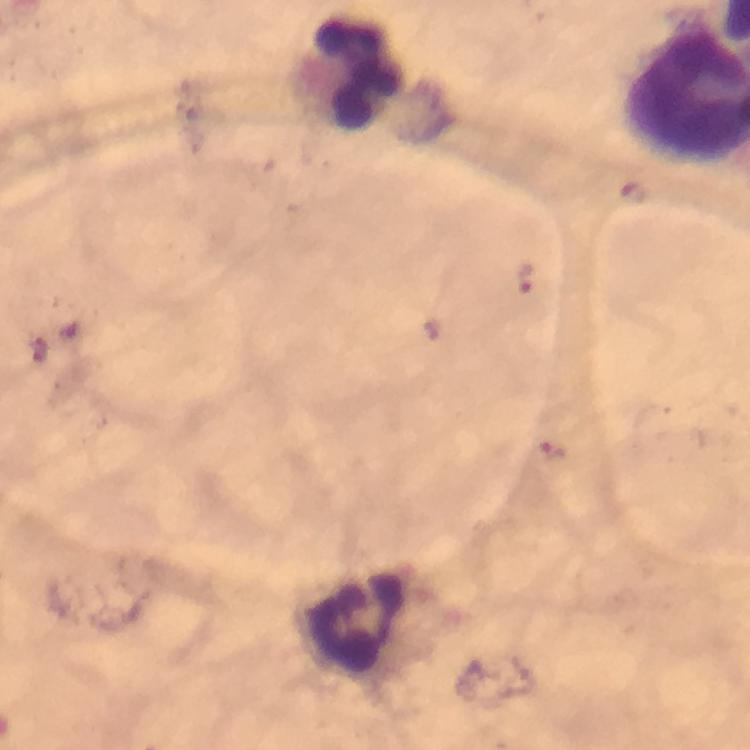
Approximate object centers, in pixels from the top-left corner.
Summary:
  - Leukocyte locations: (x=360, y=75), (x=351, y=629)
  - Malaria parasite locations: (x=525, y=277), (x=554, y=450)
  - Immersion oil: used
  - Context: from a malaria diagnostic workup
  - Magnification: 100x
  - Image size: 750×750 pixels
  - Stain: Giemsa
  - Preparation: thick blood smear
  - Cropped from: one field of view
  - Capture: smartphone photograph through a microscope